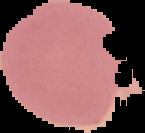

Image is 145×133 pixels. Malaria status: uninfected. From a thin blood film. Cell region segmented out of the field of view; the surrounding area is masked to black.